Assess this cell for malaria.
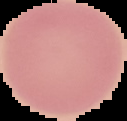
It is uninfected.

Summary:
  - Image size: 127×121 pixels
  - Image type: cell region segmented out of the field of view; surrounding area masked to black
  - Preparation: thin blood film